Describe the morphology of the red blood cells.
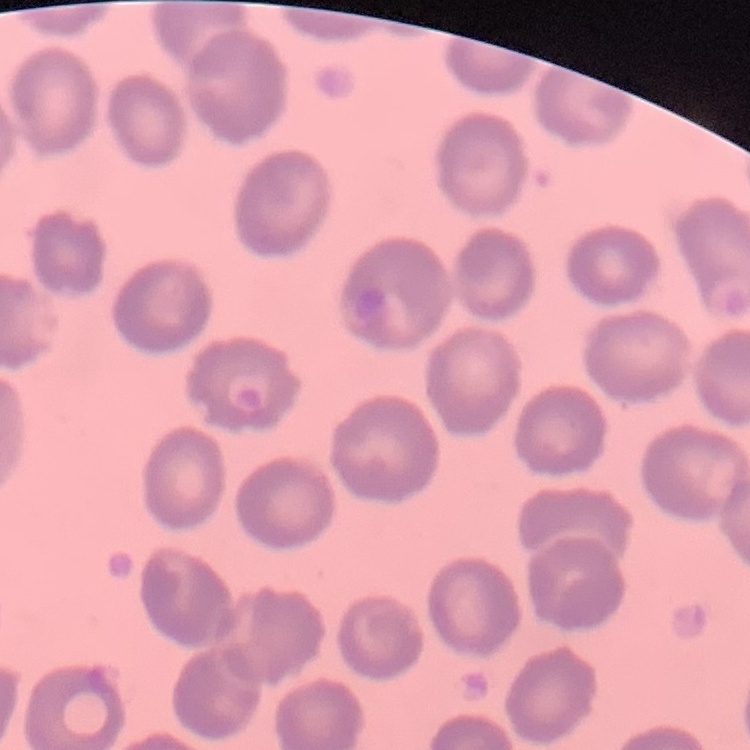

They show no rouleaux formation.

Thin blood smear. Stained with either Field's or Giemsa. One tile cut from a larger photomicrograph.